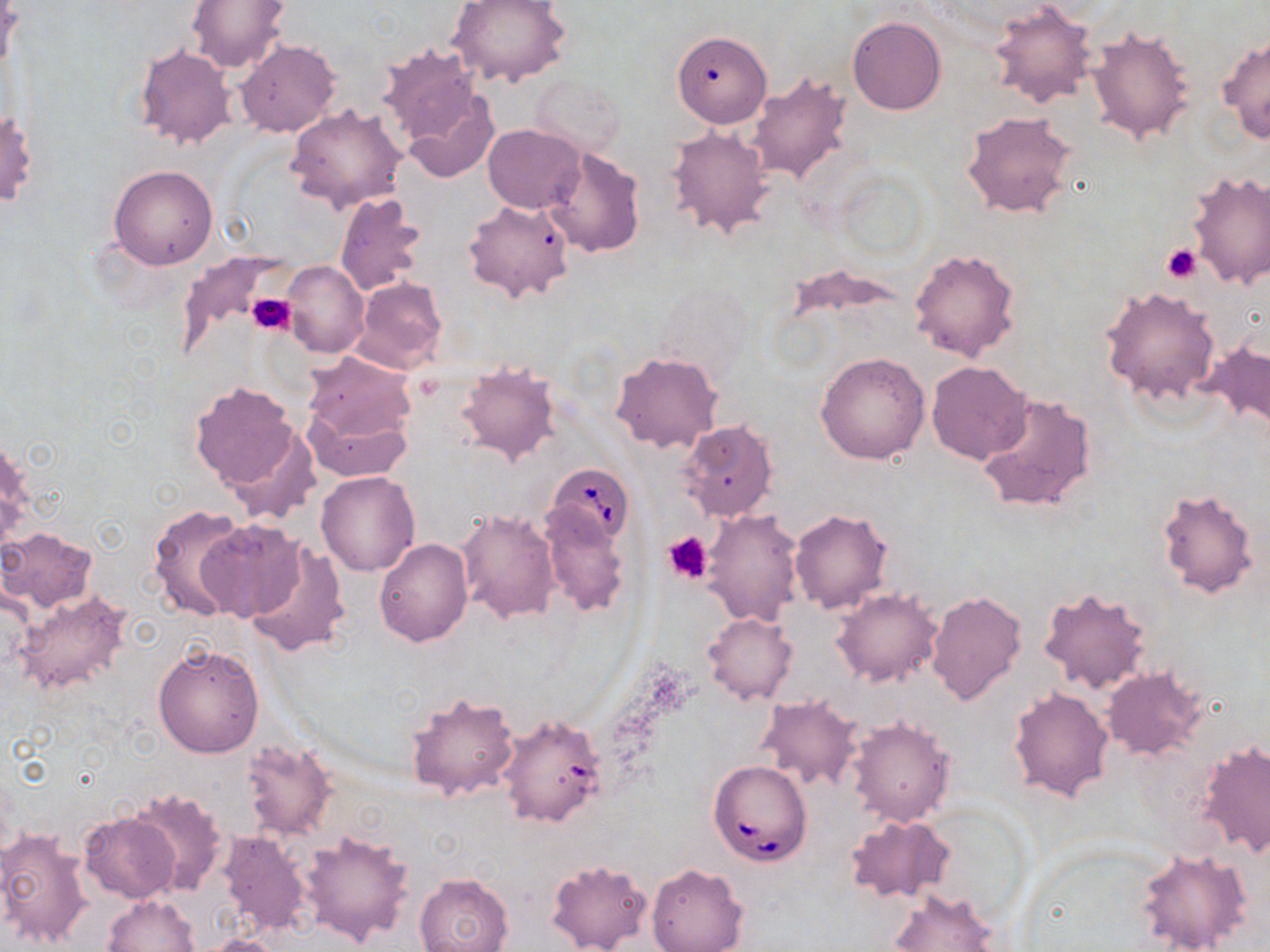
Summary:
  - Coordinate format: approximate bounding boxes as (x1,y1)-(x2,y2) corner pairs in pixels
  - Platelet locations: (1162,244)-(1201,283), (245,291)-(295,335), (663,531)-(713,585)
  - Uninfected red blood cell locations: (188,0)-(291,73), (448,0)-(574,88), (986,2)-(1098,110), (848,16)-(946,116), (1086,26)-(1196,147), (671,31)-(771,129), (1218,32)-(1270,143), (236,40)-(340,138), (375,43)-(487,151), (135,45)-(236,150), (746,72)-(856,187), (530,75)-(625,156), (400,88)-(500,183), (286,103)-(406,213), (960,109)-(1084,220), (483,124)-(584,213), (667,124)-(775,239), (544,146)-(646,258), (505,162)-(632,290), (109,165)-(218,269), (1186,171)-(1270,288), (334,192)-(428,298), (463,198)-(573,302), (177,243)-(286,362), (909,247)-(1021,365), (282,260)-(368,358), (350,275)-(449,376), (1100,286)-(1221,406), (1202,338)-(1269,432), (611,351)-(723,455), (816,351)-(930,464), (300,353)-(418,476), (454,360)-(560,466), (926,361)-(1032,466), (190,382)-(303,496), (976,391)-(1099,515), (679,419)-(778,522), (222,428)-(319,525), (315,470)-(421,577), (1155,487)-(1260,600), (538,504)-(630,618), (146,505)-(251,622), (457,508)-(561,623), (790,508)-(894,614), (703,509)-(804,627), (193,518)-(306,622), (2,527)-(97,612), (374,539)-(472,645), (243,540)-(351,657), (1039,586)-(1153,697), (12,587)-(133,699), (833,588)-(942,688), (925,589)-(1026,705), (704,612)-(796,705), (153,643)-(265,758), (1101,667)-(1207,759), (1008,687)-(1115,803), (404,691)-(520,802), (756,695)-(862,791), (497,714)-(606,828), (847,715)-(955,827), (242,739)-(336,841), (1197,742)-(1270,859), (129,787)-(227,896), (79,812)-(181,905), (845,814)-(954,902), (0,828)-(95,947), (300,828)-(415,945), (217,829)-(312,938), (1135,845)-(1253,952), (544,859)-(652,952), (645,863)-(748,952), (415,873)-(514,952), (889,889)-(998,952), (103,894)-(200,952), (204,935)-(287,952)
  - Babesia divergens-infected red blood cell locations: (547,460)-(636,548), (708,760)-(812,867)
  - Slide-level diagnosis: Babesia divergens
  - Field of view: single
  - Modality: optical microscopy
  - Preparation: thin blood film
  - Stain: May-Grünwald-Giemsa
  - Image size: 1270×952 pixels
  - Magnification: 1000x